Locate every Plasmodium falciparum parasite and identify its life-cycle stage.
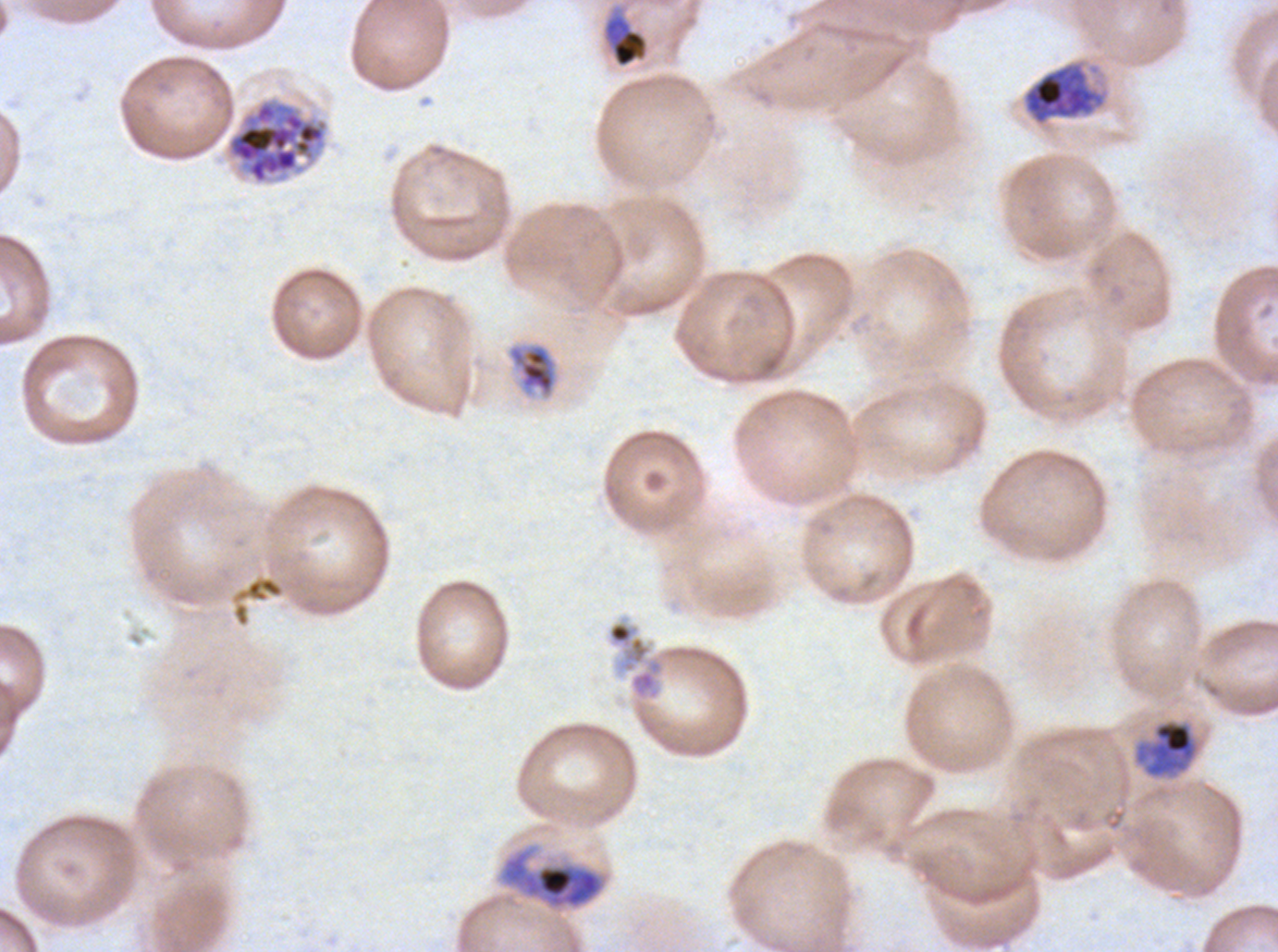
Approximate bounding boxes as (x1, y1, x2, y2) in pixels.
Late-ring/early-trophozoite forms: (604, 15, 648, 68).
Mid trophozoites: (508, 343, 557, 397).
Late trophozoites: (1020, 57, 1111, 128), (1134, 718, 1198, 778), (498, 846, 607, 910).
Late schizonts: (226, 98, 329, 185).
No rings, early schizonts, segmenters, or gametocytes observed.

Summary:
  - Debris locations: (607, 619, 666, 702)
  - Stain: Giemsa
  - Specimen: Plasmodium falciparum cultured ex vivo for 24 to 48 hours, from a patient in The Gambia
  - Life-cycle stages observed: late-ring/early-trophozoite, mid trophozoite, late trophozoite, late schizont
  - Preparation: thin blood film
  - Image size: 1278×952 pixels
  - Field of view: sub-image separated from a larger composite